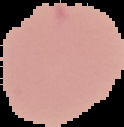

Summary:
  - Result: negative for malaria parasites
  - Image type: segmented cell region on a black background
  - Preparation: thin blood film
  - Image size: 124×127 pixels